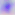

{
  "identification": "Toxoplasma gondii",
  "modality": "photomicrograph",
  "magnification": "400x"
}